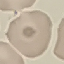
Summary:
  - Result: no malaria parasites seen
  - Stain: Giemsa
  - Image type: automatically extracted cell patch, resized to 64 × 64 pixels
  - Preparation: thin blood smear
  - Capture: smartphone through the microscope eyepiece